Name the blood parasite species.
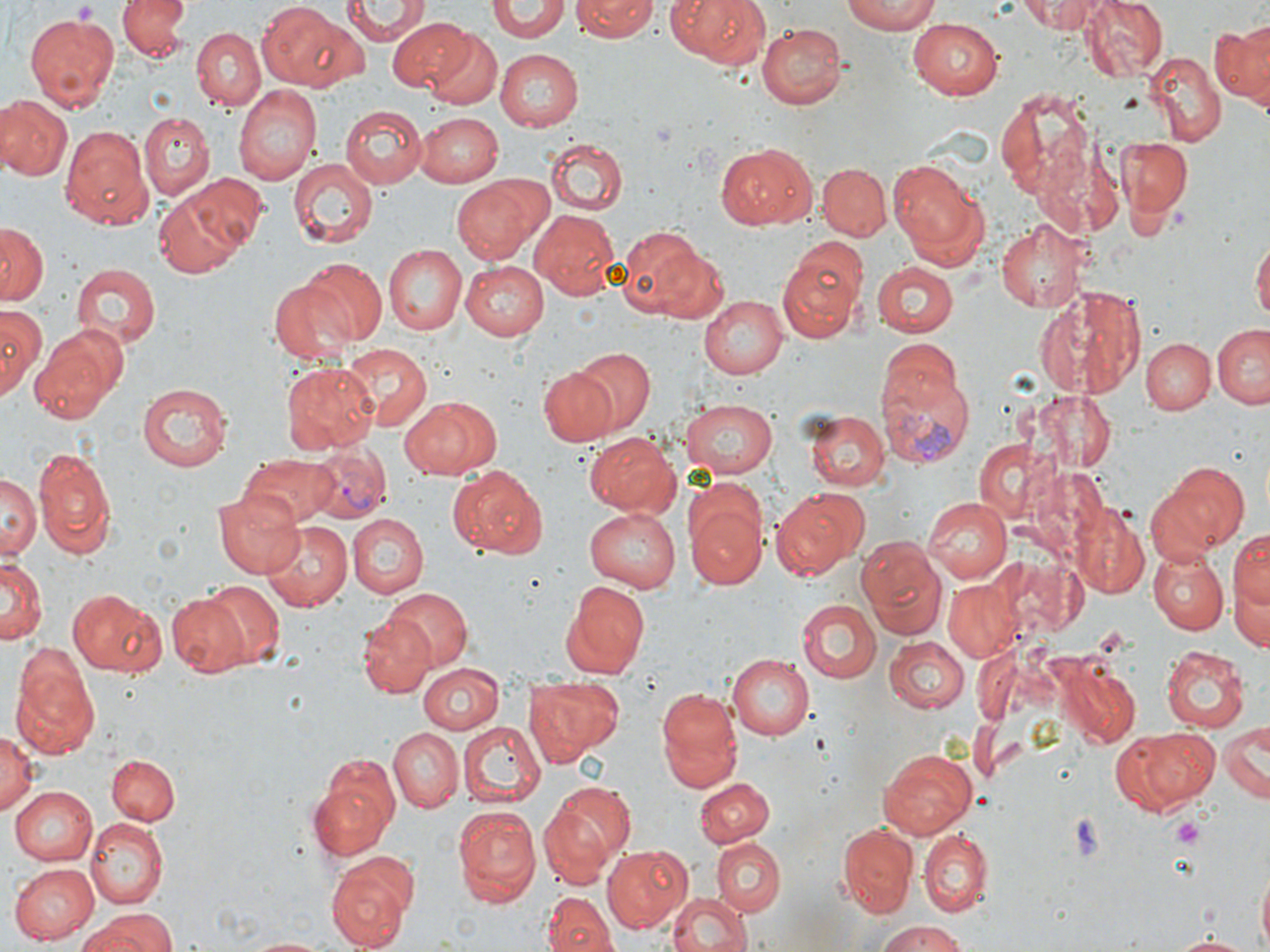

Plasmodium vivax.

Approximate bounding boxes as [x1, y1, x2, y2] in pixels. Uninfected red blood cell locations: [117, 0, 193, 63], [339, 0, 430, 44], [572, 0, 659, 41], [664, 0, 774, 70], [839, 0, 942, 34], [1017, 0, 1109, 32], [1077, 0, 1168, 82], [257, 1, 361, 92], [488, 4, 573, 42], [23, 12, 120, 110], [389, 17, 477, 93], [1214, 17, 1269, 106], [906, 19, 1005, 100], [756, 22, 847, 108], [192, 28, 265, 108], [427, 29, 504, 109], [495, 48, 586, 130], [1144, 52, 1224, 145], [234, 85, 321, 185], [997, 86, 1099, 206], [0, 94, 71, 181], [340, 105, 427, 189], [417, 111, 503, 185], [139, 112, 214, 199], [59, 125, 154, 229], [1117, 136, 1191, 218], [547, 139, 627, 215], [716, 143, 815, 230], [288, 158, 377, 248], [890, 160, 992, 273], [817, 162, 891, 239], [180, 173, 271, 257], [451, 175, 553, 267], [153, 185, 252, 278], [530, 209, 620, 298], [995, 218, 1088, 312], [0, 222, 47, 304], [619, 228, 720, 325], [1252, 233, 1269, 333], [384, 245, 467, 334], [777, 248, 868, 342], [298, 259, 387, 347], [460, 261, 548, 340], [873, 261, 958, 339], [70, 265, 157, 350], [270, 276, 361, 367], [1032, 284, 1146, 398], [700, 295, 787, 379], [0, 306, 45, 399], [1212, 325, 1270, 409], [29, 330, 118, 424], [1142, 337, 1215, 414], [879, 339, 962, 418], [343, 344, 429, 430], [574, 348, 654, 431], [280, 363, 378, 453], [537, 367, 619, 447], [136, 383, 231, 470], [1032, 390, 1118, 472], [401, 396, 500, 480], [680, 399, 783, 478], [805, 410, 889, 491], [582, 433, 679, 516], [970, 438, 1064, 529], [33, 447, 116, 557], [242, 454, 341, 525], [1154, 462, 1251, 557], [448, 465, 547, 559], [3, 474, 38, 560], [772, 487, 870, 579], [683, 488, 767, 591], [213, 491, 307, 578], [923, 497, 1012, 583], [1072, 498, 1150, 599], [585, 507, 684, 591], [345, 513, 427, 596], [259, 520, 353, 613], [1230, 523, 1269, 627], [856, 535, 945, 638], [1150, 550, 1228, 633], [0, 558, 44, 648], [1225, 565, 1270, 656], [560, 579, 650, 677], [201, 580, 286, 668], [943, 582, 1018, 660], [385, 587, 472, 670], [67, 589, 166, 675], [166, 594, 249, 676], [797, 598, 881, 685], [358, 614, 437, 698], [883, 636, 969, 712], [1159, 643, 1251, 733], [725, 651, 814, 738], [10, 652, 99, 759], [417, 662, 505, 734], [1061, 668, 1140, 748], [524, 675, 622, 760], [655, 685, 744, 794], [455, 721, 543, 808], [1218, 722, 1266, 806], [387, 726, 462, 812], [1116, 726, 1218, 812], [0, 729, 39, 816], [877, 748, 976, 838], [108, 756, 178, 825], [310, 761, 398, 861], [694, 777, 773, 848], [544, 778, 636, 875], [9, 786, 99, 865], [452, 805, 541, 907], [84, 818, 165, 910], [836, 823, 916, 915], [920, 831, 992, 916], [713, 839, 786, 916], [603, 844, 692, 932], [325, 848, 419, 952], [9, 862, 100, 943], [1254, 868, 1269, 952], [664, 891, 754, 952], [544, 892, 614, 952], [79, 909, 179, 952], [871, 919, 969, 952], [1166, 933, 1256, 950], [245, 935, 340, 952]. Plasmodium vivax-infected red blood cell locations: [877, 367, 976, 469], [303, 446, 390, 524]. Platelet locations: [70, 2, 99, 22], [1065, 813, 1107, 860], [1170, 816, 1206, 846]. Image is 1270×952 pixels. Captured at 1000x magnification. Single field of view. Optical microscopy. May-Grünwald-Giemsa-stained preparation. Thin blood film.